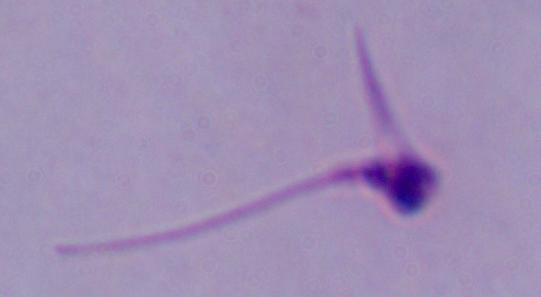
A Leishmania parasite is shown. Micrograph. 1000x magnification.